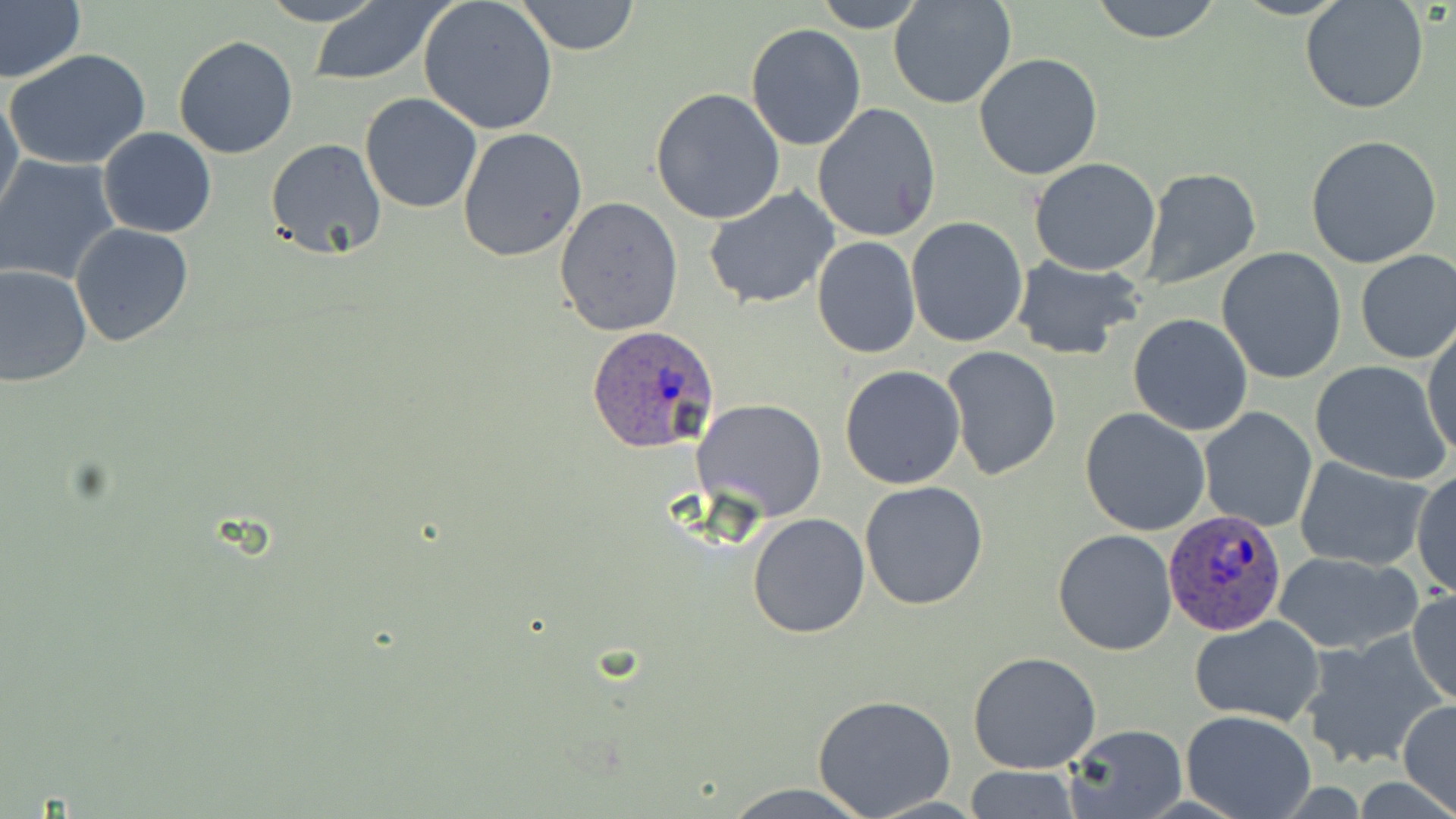
Summary:
  - Coordinate format: approximate bounding boxes as (x1, y1, x2, y2) in pixels
  - Plasmodium ovale-infected red blood cell locations: (587, 327, 721, 454), (1165, 510, 1286, 637)
  - Uninfected red blood cell locations: (0, 0, 85, 87), (257, 0, 387, 25), (417, 0, 560, 135), (810, 0, 929, 32), (889, 0, 1018, 109), (1088, 0, 1225, 44), (1301, 0, 1430, 116), (515, 1, 640, 55), (306, 2, 452, 86), (745, 23, 867, 151), (173, 34, 301, 158), (6, 49, 153, 171), (973, 54, 1103, 180), (649, 88, 785, 226), (0, 89, 24, 224), (359, 92, 482, 214), (812, 102, 942, 242), (98, 127, 217, 238), (458, 128, 588, 263), (1304, 134, 1442, 268), (263, 139, 388, 262), (0, 156, 122, 285), (1029, 158, 1161, 276), (1137, 167, 1262, 289), (704, 187, 842, 312), (554, 197, 683, 336), (906, 217, 1029, 348), (69, 223, 195, 348), (811, 235, 921, 358), (1216, 247, 1347, 383), (1355, 250, 1456, 364), (1010, 255, 1143, 359), (0, 263, 92, 388), (1128, 313, 1253, 435), (1424, 322, 1456, 465), (941, 347, 1064, 482), (1309, 360, 1452, 485), (840, 364, 967, 489), (694, 397, 828, 522), (1199, 407, 1318, 532), (1080, 408, 1211, 536), (1293, 455, 1433, 568), (1412, 469, 1455, 597), (860, 481, 988, 611), (748, 513, 870, 639), (1053, 528, 1177, 656), (1271, 549, 1423, 655), (1407, 589, 1455, 707), (1189, 615, 1326, 726), (1298, 631, 1448, 771), (969, 651, 1102, 774), (810, 695, 957, 817), (1398, 700, 1456, 814), (1180, 711, 1316, 819), (1059, 723, 1188, 819), (964, 766, 1082, 818), (716, 781, 883, 818), (863, 795, 989, 817)
  - Slide-level diagnosis: Plasmodium ovale
  - Magnification: 1000x
  - Preparation: thin blood film
  - Field of view: single
  - Modality: light microscopy
  - Image size: 1456×819 pixels
  - Stain: May-Grünwald-Giemsa